Classify this cell by malaria status.
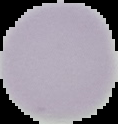

It is uninfected.

From a thin blood smear. Image is 118×124 pixels. Segmented cell region on a black background.